Assess this cell for malaria.
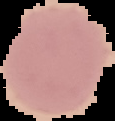
Uninfected.

From a thin blood smear. Cell region segmented out of the field of view; the surrounding area is masked to black. Image is 115×121 pixels.